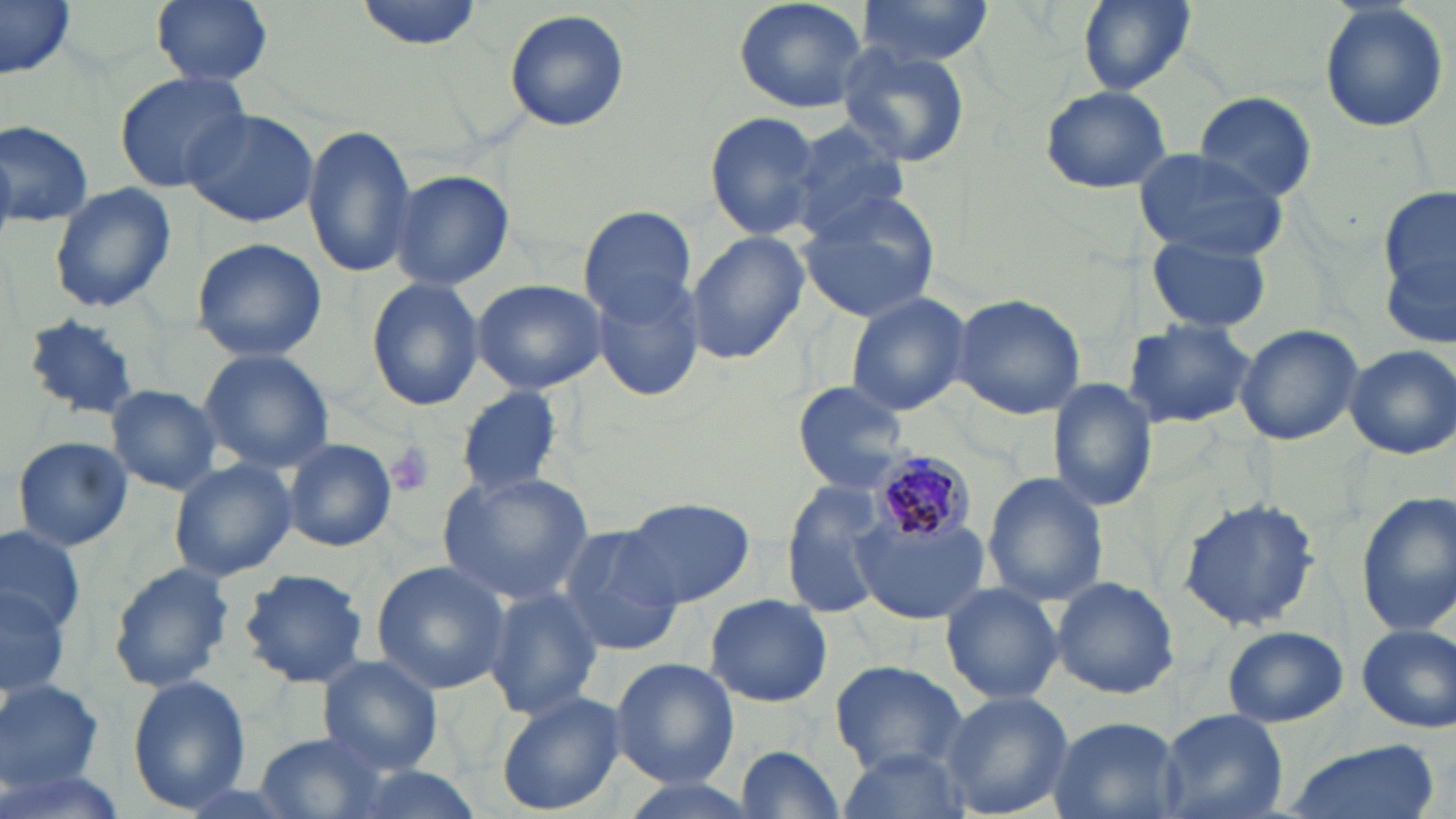

Approximate bounding boxes as [x1, y1, x2, y2] in pixels. Platelet locations: [384, 443, 436, 496]. Plasmodium malariae-infected red blood cell locations: [869, 447, 971, 553]. Uninfected red blood cell locations: [0, 0, 75, 77], [151, 0, 274, 87], [352, 0, 485, 50], [733, 0, 870, 114], [858, 0, 996, 67], [1077, 0, 1193, 92], [1316, 0, 1452, 135], [503, 8, 630, 135], [835, 45, 969, 168], [114, 69, 253, 193], [1038, 86, 1172, 195], [1194, 91, 1318, 202], [182, 106, 319, 229], [705, 109, 826, 243], [783, 118, 913, 239], [0, 119, 93, 230], [301, 123, 418, 277], [1134, 149, 1287, 259], [389, 169, 514, 292], [47, 182, 177, 315], [1380, 183, 1456, 335], [797, 191, 943, 322], [578, 207, 696, 321], [1147, 232, 1277, 336], [685, 233, 809, 364], [190, 238, 328, 362], [591, 274, 704, 401], [471, 278, 606, 394], [366, 279, 484, 411], [844, 290, 972, 417], [952, 295, 1085, 421], [19, 312, 148, 418], [1122, 320, 1256, 430], [1235, 322, 1365, 446], [1343, 343, 1456, 459], [198, 349, 334, 472], [1048, 378, 1158, 512], [792, 381, 910, 494], [105, 385, 222, 495], [453, 389, 563, 497], [10, 435, 134, 552], [281, 437, 398, 551], [168, 459, 297, 582], [437, 471, 595, 604], [983, 471, 1105, 607], [782, 482, 890, 616], [1355, 494, 1456, 636], [616, 497, 757, 607], [1178, 497, 1321, 633], [850, 513, 990, 623], [552, 525, 683, 657], [0, 528, 84, 636], [370, 560, 514, 692], [106, 563, 235, 693], [238, 568, 369, 687], [1052, 576, 1180, 698], [940, 581, 1064, 705], [0, 582, 71, 704], [484, 586, 603, 719], [704, 594, 833, 708], [1354, 621, 1456, 734], [1221, 626, 1348, 727], [318, 656, 444, 774], [610, 658, 738, 788], [831, 660, 967, 774], [126, 676, 252, 811], [0, 679, 104, 790], [938, 689, 1074, 818], [495, 690, 626, 816], [1159, 708, 1287, 819], [1049, 713, 1183, 819], [255, 731, 389, 817], [1284, 738, 1439, 819], [735, 744, 846, 816], [835, 748, 971, 819], [0, 756, 127, 819], [610, 774, 762, 819]. Slide-level diagnosis: Plasmodium malariae. Light microscopy. May-Grünwald-Giemsa-stained preparation. Thin blood smear. Image is 1456×819 pixels. Captured at 1000x magnification. Single field of view.